Locate every malaria parasite.
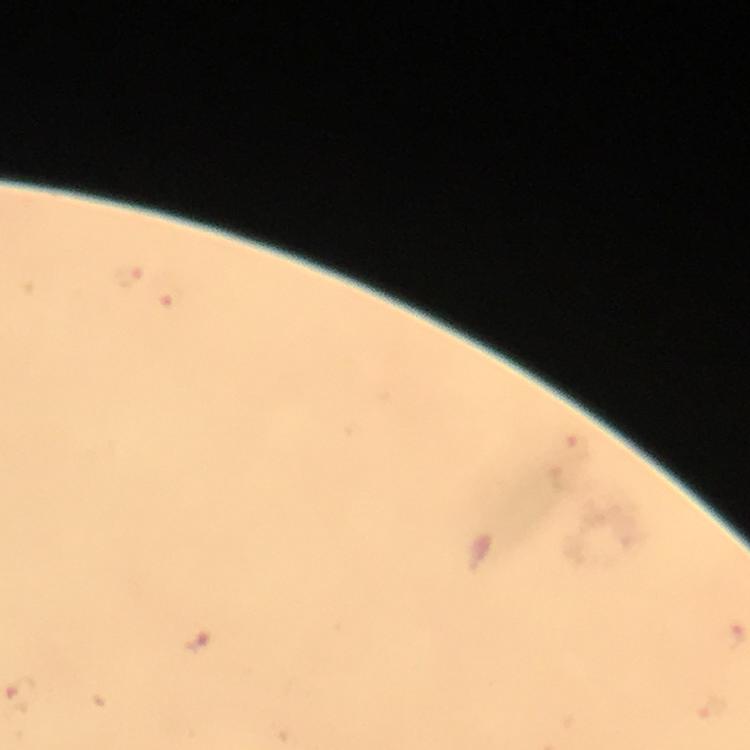

Approximate object centers, in pixels from the top-left corner.
Malaria parasites: (x=129, y=275), (x=169, y=299), (x=199, y=639).

Summary:
  - Immersion oil: applied
  - Capture: smartphone camera through the microscope
  - Magnification: 100x
  - Image size: 750×750 pixels
  - Context: from a diagnostic examination for malaria
  - Cropped from: a single field of view
  - Preparation: thick smear
  - Stain: Giemsa